Classify this cell by malaria status.
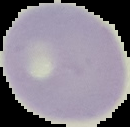

Uninfected.

image type = segmented cell region with the area outside set to black
preparation = thin blood film
image size = 130×127 pixels